Describe the morphology of the erythrocytes.
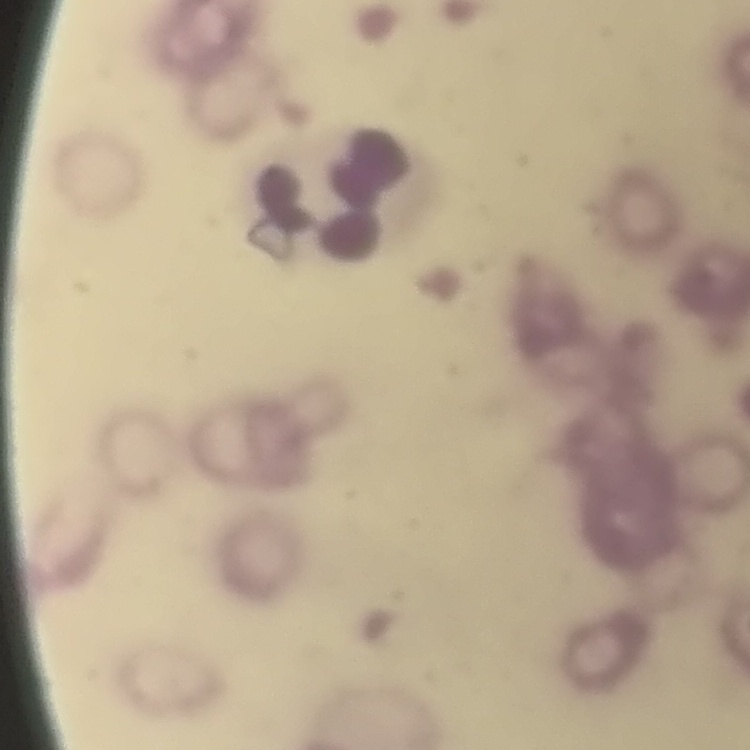

They show rouleaux formation.

Summary:
  - Preparation: thin peripheral smear
  - Image type: square crop of a larger photomicrograph
  - Stain: Field's or Giemsa